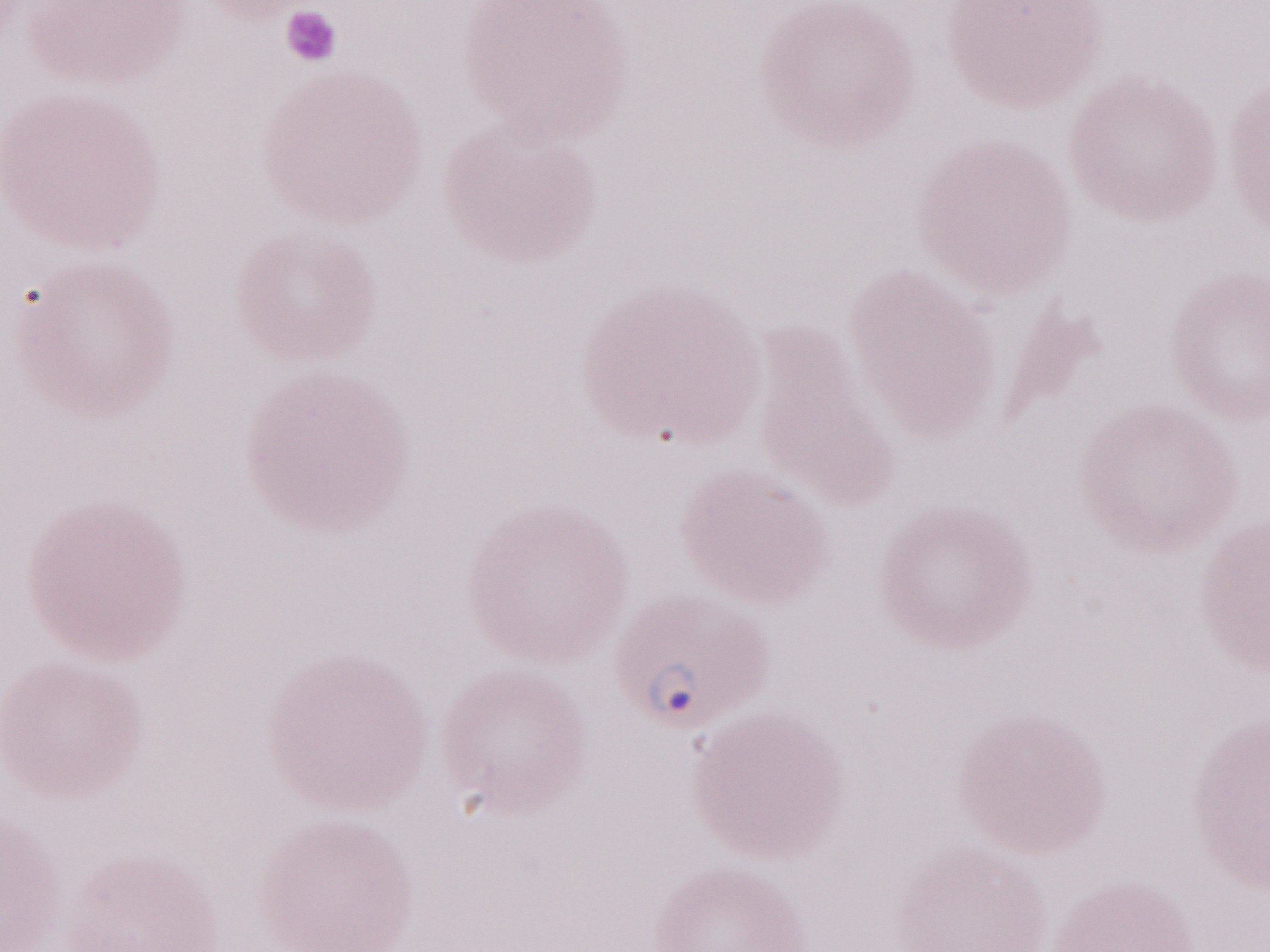 Malaria diagnosis (patient-level): positive. Image is 1270×952 pixels. Single field of view. 1,000x magnification. Olympus BX43 microscope, Olympus DP73 camera. Thin peripheral-blood smear. May-Grünwald-Giemsa (MGG) stain.